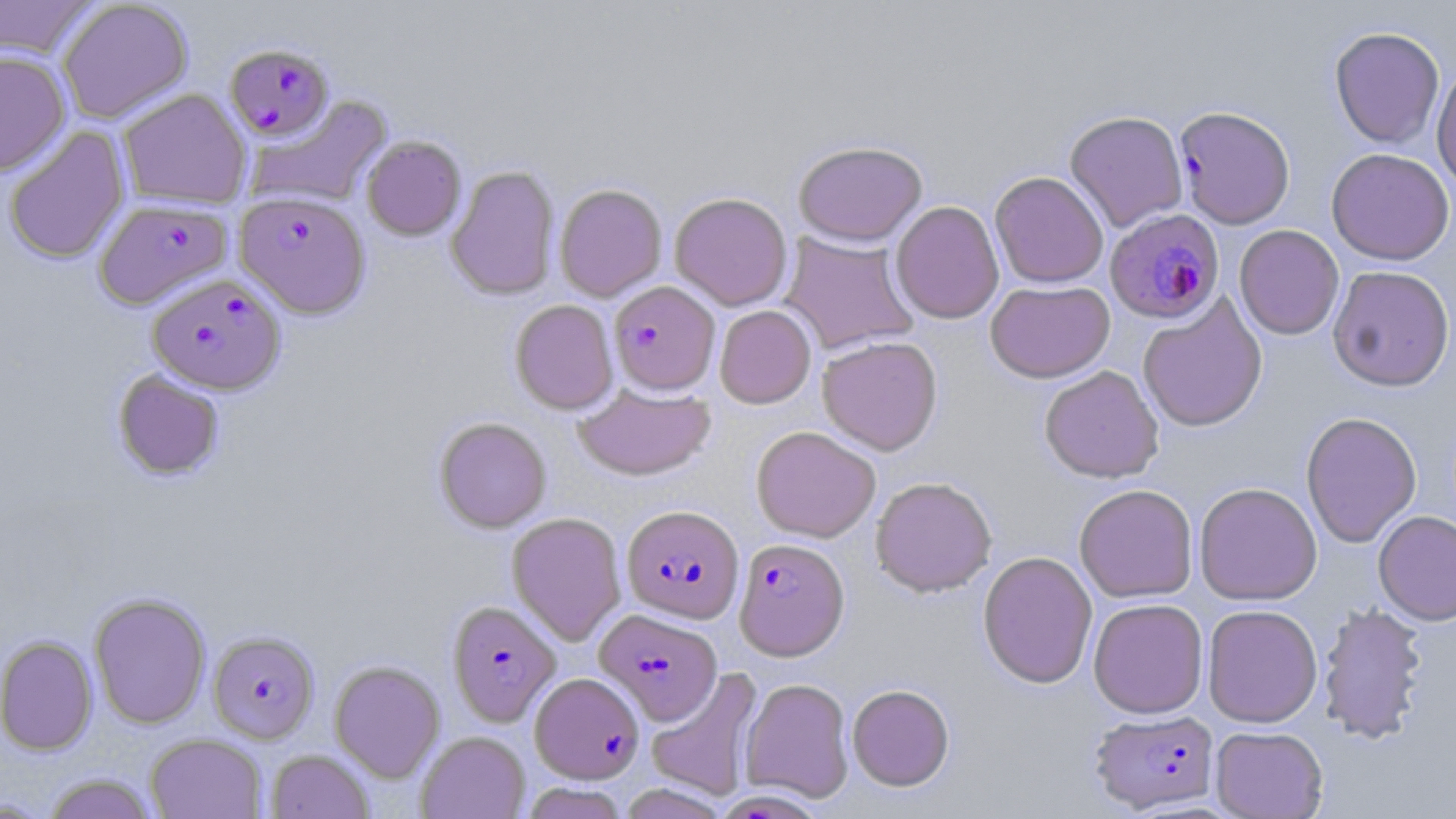 Approximate bounding boxes as [x1, y1, x2, y2] in pixels. Plasmodium falciparum-infected red blood cell locations: [225, 44, 335, 141], [1174, 105, 1296, 230], [234, 192, 370, 318], [94, 198, 232, 310], [1105, 208, 1225, 325], [147, 273, 286, 394], [609, 280, 720, 395], [621, 505, 744, 622], [734, 537, 849, 660], [446, 600, 561, 726], [596, 609, 722, 725], [208, 630, 320, 743], [529, 675, 643, 786], [1089, 709, 1220, 813]. Uninfected red blood cell locations: [0, 0, 101, 62], [57, 1, 193, 124], [1329, 25, 1445, 150], [0, 50, 70, 177], [1431, 61, 1456, 192], [117, 89, 251, 210], [245, 95, 393, 209], [1064, 110, 1188, 233], [3, 126, 131, 264], [361, 135, 466, 240], [793, 139, 927, 246], [1327, 147, 1455, 265], [445, 165, 560, 300], [989, 170, 1108, 288], [554, 183, 667, 302], [669, 192, 793, 310], [891, 200, 1005, 325], [1234, 224, 1344, 340], [779, 231, 920, 355], [1327, 265, 1455, 391], [985, 279, 1115, 383], [1138, 296, 1267, 432], [510, 299, 618, 414], [714, 305, 816, 409], [817, 336, 943, 455], [1039, 365, 1164, 483], [112, 369, 224, 480], [574, 384, 717, 480], [1300, 411, 1422, 548], [434, 417, 551, 533], [750, 426, 881, 542], [870, 476, 998, 597], [1194, 481, 1322, 606], [1074, 484, 1198, 603], [1373, 510, 1456, 626], [507, 512, 627, 646], [977, 551, 1098, 688], [88, 593, 211, 729], [1088, 598, 1209, 718], [1316, 602, 1430, 745], [1202, 604, 1323, 728], [0, 636, 97, 755], [329, 660, 445, 782], [646, 668, 763, 802], [740, 678, 854, 803], [847, 684, 955, 791], [1210, 726, 1329, 818], [417, 731, 530, 818], [146, 733, 266, 819], [266, 748, 374, 819], [41, 773, 160, 819], [519, 782, 630, 819], [0, 796, 57, 818]. Slide-level diagnosis: Plasmodium falciparum. 1000x magnification. Single field of view. May-Grünwald-Giemsa stain. Image is 1456×819 pixels. Thin blood smear. Light microscopy.